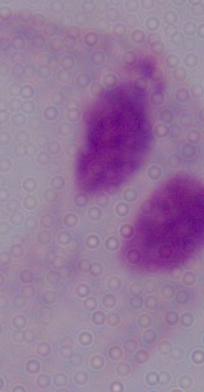
{
  "identification": "trichomonad",
  "magnification": "1000x",
  "modality": "micrograph"
}